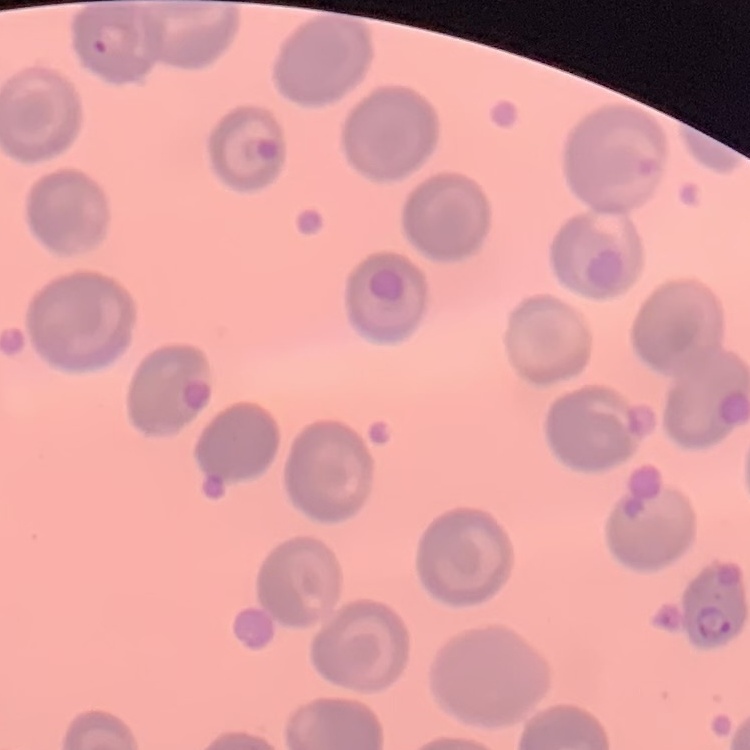

Summary:
  - Red blood cell morphology: no rouleaux formation
  - Preparation: thin peripheral smear
  - Image type: square crop of a larger photomicrograph
  - Stain: Field's or Giemsa